Describe the morphology of the erythrocytes.
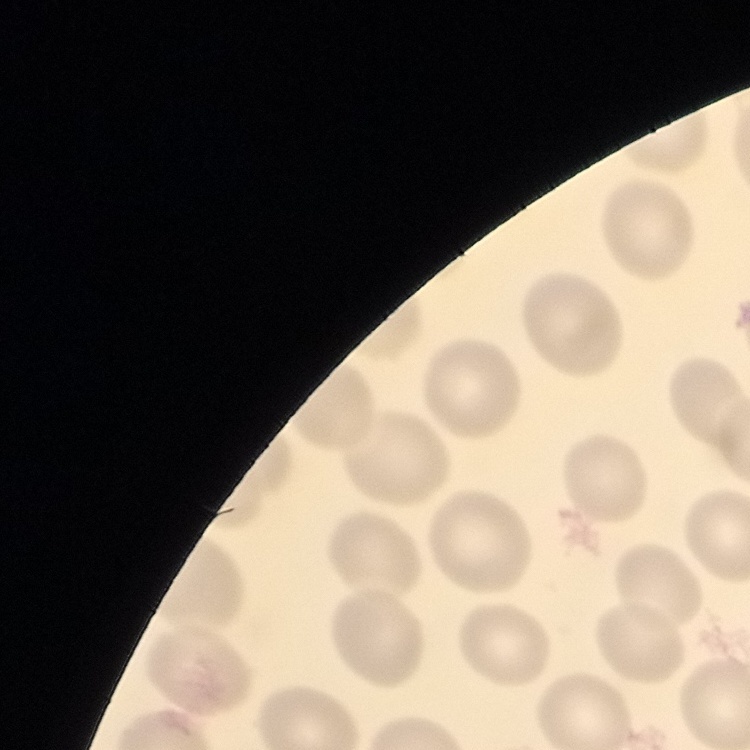
They show no rouleaux formation.

image type = one tile cut from a larger photomicrograph
preparation = thin blood film
stain = Field's or Giemsa